Identify the parasite.
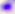
Toxoplasma gondii.

400x magnification. Photomicrograph.